Assess the morphology of the red blood cells.
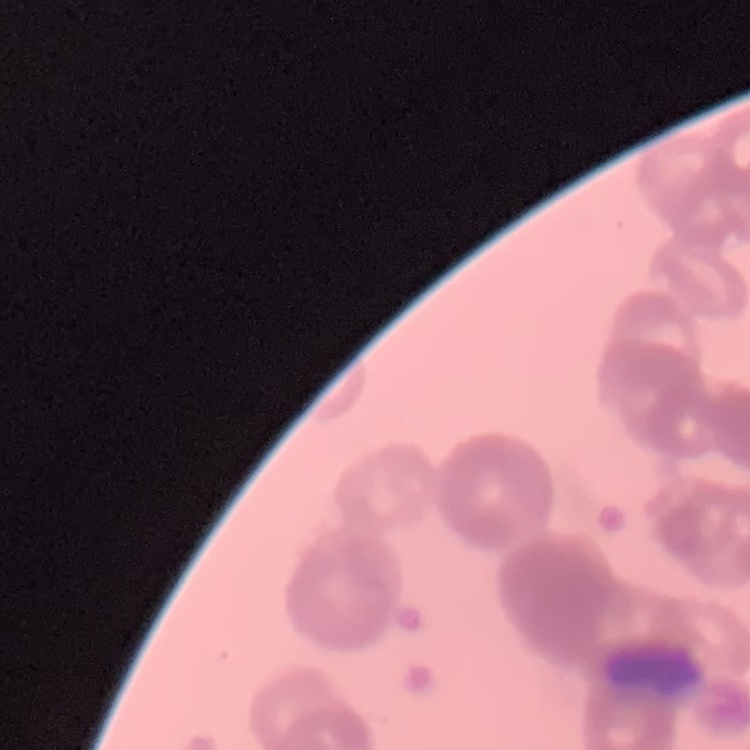
They show rouleaux formation.

Stained with either Field's or Giemsa. Thin blood smear. Square crop of a larger photomicrograph.